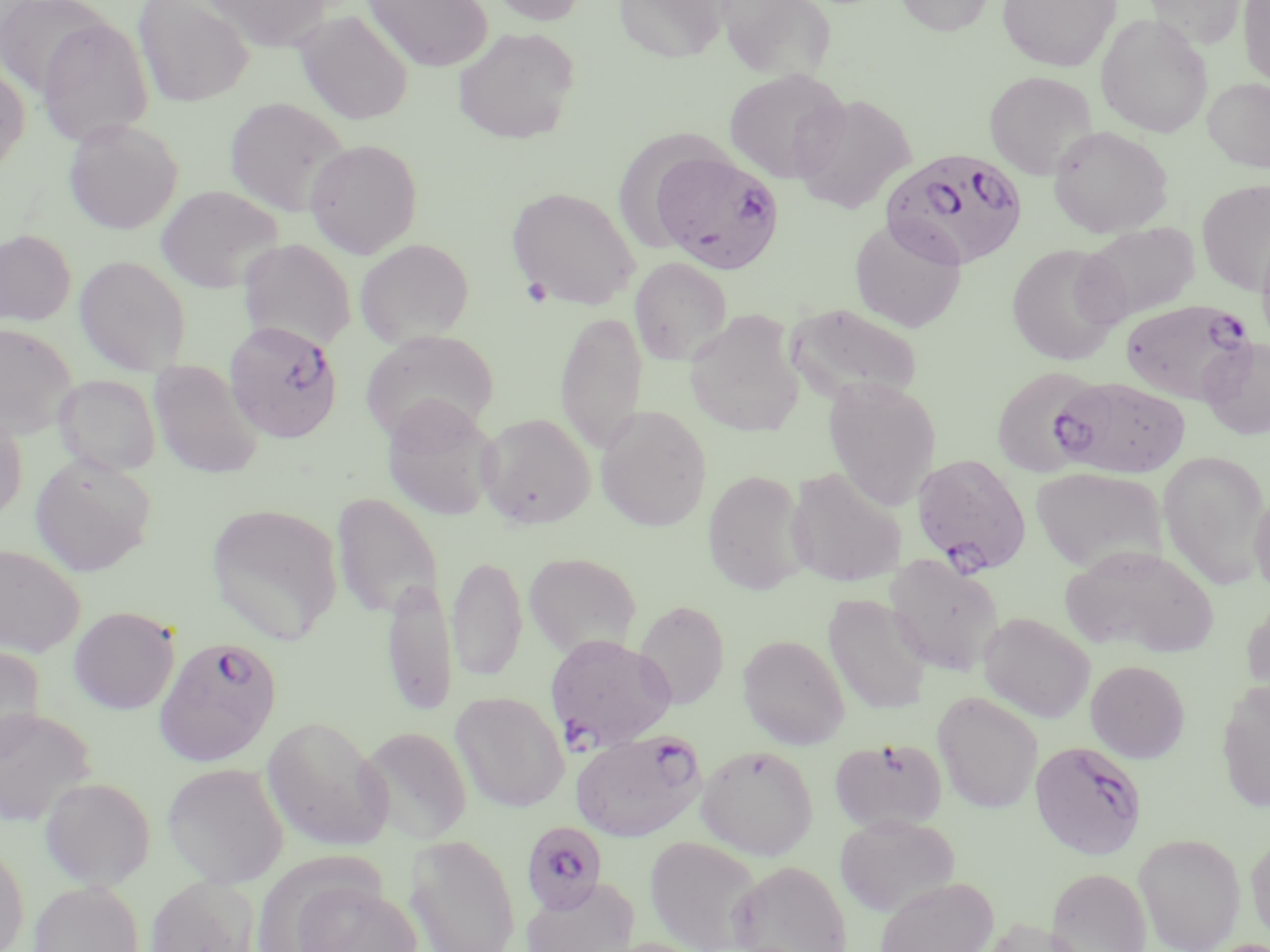
Approximate bounding boxes as named x1/y1/x2/y2 corners in pixels. Uninfected red blood cell locations: (x1=0, y1=0, x2=111, y2=98), (x1=133, y1=0, x2=254, y2=107), (x1=363, y1=0, x2=492, y2=71), (x1=486, y1=0, x2=589, y2=25), (x1=613, y1=0, x2=730, y2=62), (x1=718, y1=0, x2=837, y2=82), (x1=895, y1=0, x2=994, y2=35), (x1=998, y1=0, x2=1120, y2=71), (x1=1142, y1=0, x2=1249, y2=49), (x1=1238, y1=0, x2=1270, y2=88), (x1=199, y1=1, x2=336, y2=52), (x1=294, y1=9, x2=414, y2=125), (x1=1095, y1=13, x2=1213, y2=138), (x1=36, y1=18, x2=154, y2=146), (x1=453, y1=26, x2=580, y2=145), (x1=0, y1=61, x2=30, y2=177), (x1=724, y1=67, x2=850, y2=183), (x1=984, y1=71, x2=1097, y2=179), (x1=1203, y1=77, x2=1270, y2=172), (x1=791, y1=93, x2=916, y2=214), (x1=224, y1=96, x2=350, y2=216), (x1=64, y1=118, x2=183, y2=234), (x1=1048, y1=125, x2=1173, y2=237), (x1=304, y1=138, x2=423, y2=258), (x1=1196, y1=180, x2=1270, y2=293), (x1=156, y1=185, x2=283, y2=293), (x1=506, y1=186, x2=641, y2=310), (x1=849, y1=217, x2=967, y2=332), (x1=1080, y1=222, x2=1201, y2=321), (x1=0, y1=229, x2=76, y2=326), (x1=1257, y1=234, x2=1270, y2=349), (x1=238, y1=238, x2=355, y2=352), (x1=355, y1=238, x2=474, y2=348), (x1=1006, y1=243, x2=1125, y2=365), (x1=74, y1=255, x2=191, y2=375), (x1=629, y1=257, x2=733, y2=365), (x1=787, y1=303, x2=922, y2=404), (x1=555, y1=310, x2=647, y2=456), (x1=684, y1=310, x2=806, y2=437), (x1=0, y1=322, x2=79, y2=438), (x1=361, y1=329, x2=499, y2=443), (x1=1199, y1=337, x2=1270, y2=441), (x1=149, y1=360, x2=263, y2=479), (x1=991, y1=365, x2=1104, y2=476), (x1=53, y1=374, x2=161, y2=476), (x1=823, y1=377, x2=942, y2=510), (x1=381, y1=395, x2=500, y2=522), (x1=595, y1=405, x2=712, y2=532), (x1=0, y1=408, x2=27, y2=522), (x1=476, y1=412, x2=596, y2=529), (x1=1157, y1=449, x2=1270, y2=589), (x1=29, y1=453, x2=156, y2=577), (x1=786, y1=466, x2=907, y2=587), (x1=1030, y1=466, x2=1166, y2=575), (x1=702, y1=469, x2=810, y2=595), (x1=1249, y1=489, x2=1270, y2=596), (x1=331, y1=493, x2=444, y2=619), (x1=206, y1=502, x2=344, y2=644), (x1=0, y1=543, x2=86, y2=657), (x1=1058, y1=544, x2=1219, y2=658), (x1=523, y1=551, x2=642, y2=659), (x1=884, y1=553, x2=1004, y2=676), (x1=447, y1=554, x2=527, y2=682), (x1=382, y1=575, x2=458, y2=716), (x1=823, y1=594, x2=933, y2=715), (x1=1241, y1=594, x2=1270, y2=703), (x1=633, y1=600, x2=730, y2=710), (x1=69, y1=606, x2=180, y2=714), (x1=978, y1=611, x2=1096, y2=723), (x1=737, y1=634, x2=850, y2=749), (x1=0, y1=644, x2=45, y2=762), (x1=1085, y1=660, x2=1190, y2=763), (x1=1216, y1=680, x2=1270, y2=813), (x1=450, y1=691, x2=568, y2=812), (x1=932, y1=691, x2=1043, y2=813), (x1=0, y1=706, x2=96, y2=827), (x1=262, y1=715, x2=393, y2=852), (x1=359, y1=726, x2=472, y2=844), (x1=830, y1=736, x2=947, y2=833), (x1=696, y1=745, x2=818, y2=860), (x1=162, y1=762, x2=289, y2=888), (x1=40, y1=776, x2=156, y2=890), (x1=834, y1=814, x2=960, y2=917), (x1=1133, y1=832, x2=1246, y2=952), (x1=404, y1=833, x2=521, y2=952), (x1=1245, y1=833, x2=1270, y2=945), (x1=645, y1=835, x2=764, y2=952), (x1=0, y1=842, x2=29, y2=952), (x1=729, y1=860, x2=851, y2=952), (x1=1047, y1=867, x2=1152, y2=952), (x1=145, y1=875, x2=259, y2=952), (x1=521, y1=876, x2=640, y2=952), (x1=874, y1=876, x2=998, y2=952), (x1=29, y1=880, x2=144, y2=952), (x1=293, y1=881, x2=424, y2=952), (x1=975, y1=917, x2=1088, y2=952). Plasmodium falciparum-infected red blood cell locations: (x1=881, y1=148, x2=1029, y2=271), (x1=653, y1=150, x2=783, y2=273), (x1=1121, y1=299, x2=1255, y2=403), (x1=220, y1=322, x2=345, y2=447), (x1=1050, y1=376, x2=1190, y2=478), (x1=911, y1=454, x2=1032, y2=575), (x1=544, y1=633, x2=676, y2=751), (x1=154, y1=636, x2=282, y2=767), (x1=570, y1=728, x2=706, y2=842), (x1=1029, y1=739, x2=1147, y2=861), (x1=518, y1=822, x2=611, y2=934). Platelet locations: (x1=522, y1=276, x2=552, y2=308). Slide-level diagnosis: Plasmodium falciparum. Captured at 1000x magnification. Image is 1270×952 pixels. Light microscopy. May-Grünwald-Giemsa-stained preparation. Thin blood film. Single field of view.